Report the malaria status of this cell.
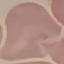

It is uninfected.

preparation = thin blood smear
capture = smartphone camera at the microscope eyepiece
stain = Giemsa
image type = automatically extracted cell patch, resized to 64 × 64 pixels